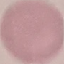
Summary:
  - Malaria status: uninfected
  - Stain: Giemsa
  - Capture: smartphone through the microscope eyepiece
  - Preparation: thin blood film
  - Image type: automatically extracted cell patch, resized to 64 × 64 pixels